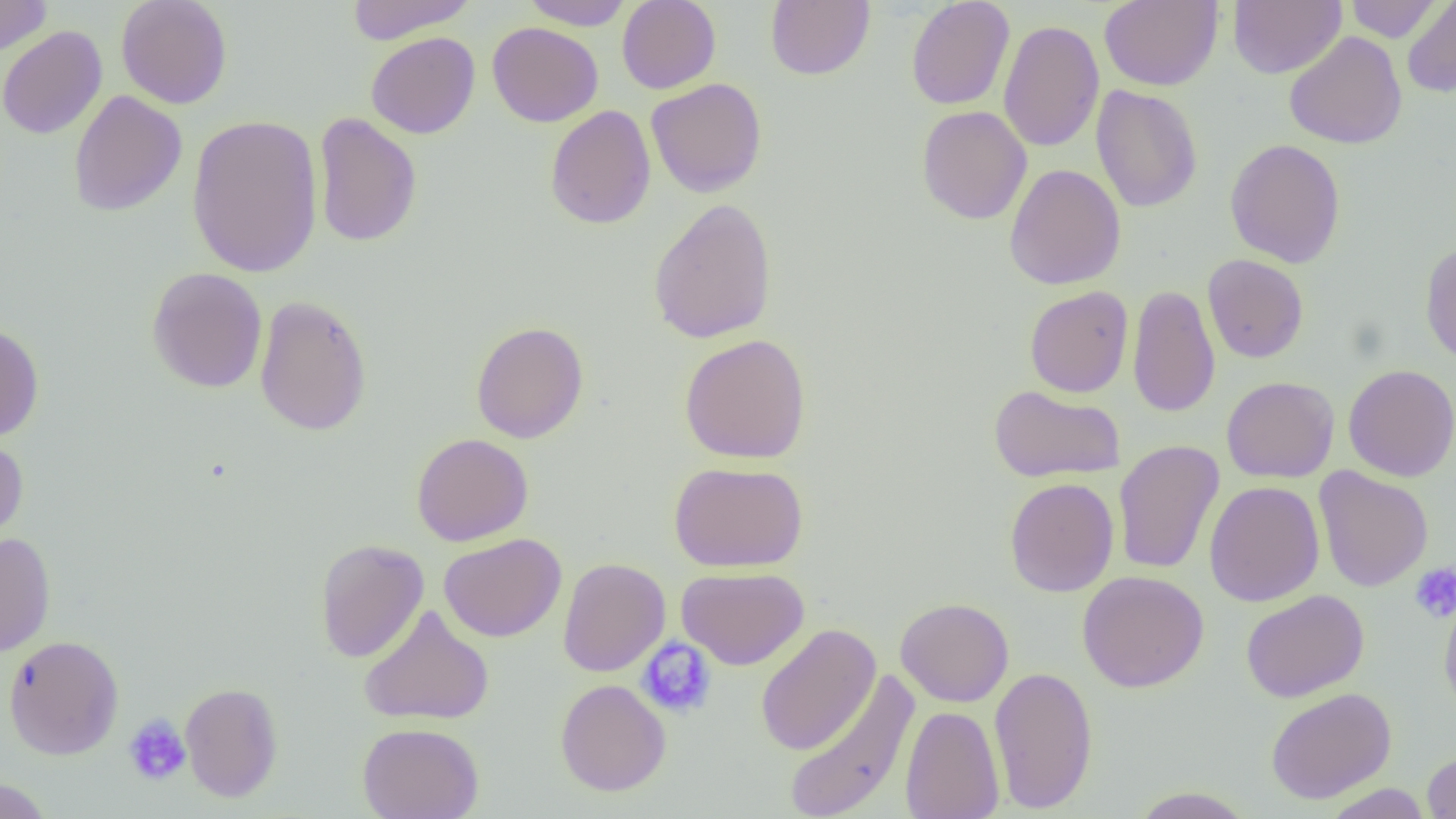 Approximate bounding boxes as (x1,y1)-(x2,y2) corner pairs in pixels. Uninfected red blood cell locations: (0,0)-(52,59), (116,0)-(233,109), (346,0)-(477,44), (617,0)-(721,94), (765,0)-(875,80), (906,0)-(1015,110), (1099,0)-(1223,91), (1229,0)-(1346,79), (1345,0)-(1442,42), (522,1)-(634,31), (1401,1)-(1456,98), (998,20)-(1104,152), (487,22)-(603,127), (0,25)-(107,140), (1283,30)-(1408,149), (366,31)-(480,139), (646,78)-(767,197), (1091,85)-(1203,213), (69,90)-(187,216), (545,104)-(656,230), (917,105)-(1032,225), (313,112)-(422,248), (186,114)-(323,279), (1225,138)-(1346,268), (1004,163)-(1126,290), (648,198)-(778,344), (1419,241)-(1456,366), (1202,254)-(1309,363), (147,267)-(268,394), (1128,283)-(1220,418), (1024,286)-(1133,397), (254,295)-(372,437), (471,321)-(589,444), (0,322)-(44,442), (679,333)-(812,464), (1343,364)-(1456,482), (1222,376)-(1339,483), (988,384)-(1125,483), (411,432)-(533,546), (0,436)-(29,546), (1113,440)-(1224,575), (669,461)-(808,571), (1314,466)-(1433,592), (1004,477)-(1119,597), (1204,481)-(1325,607), (0,532)-(56,656), (439,533)-(567,642), (314,539)-(429,663), (558,558)-(670,677), (676,566)-(809,670), (1077,570)-(1209,692), (1439,588)-(1456,719), (1241,589)-(1369,702), (895,597)-(1014,707), (358,604)-(494,726), (755,623)-(881,757), (3,634)-(124,760), (988,665)-(1098,814), (781,669)-(920,819), (555,678)-(671,796), (180,682)-(283,802), (1265,687)-(1396,805), (900,705)-(1004,819), (357,722)-(484,819), (1422,751)-(1456,818), (0,778)-(54,819), (1321,783)-(1434,818), (1128,786)-(1256,818). Platelet locations: (1409,562)-(1456,623), (636,638)-(718,718), (123,714)-(192,787). Slide-level diagnosis: no evidence of blood parasites. Light microscopy. Thin blood smear. Image is 1456×819 pixels. 1000x magnification. One field of a larger specimen.